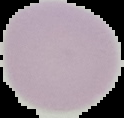

{
  "image_size": "124×118 pixels",
  "image_type": "segmented cell region on a black background",
  "malaria_status": "uninfected",
  "preparation": "thin blood smear"
}